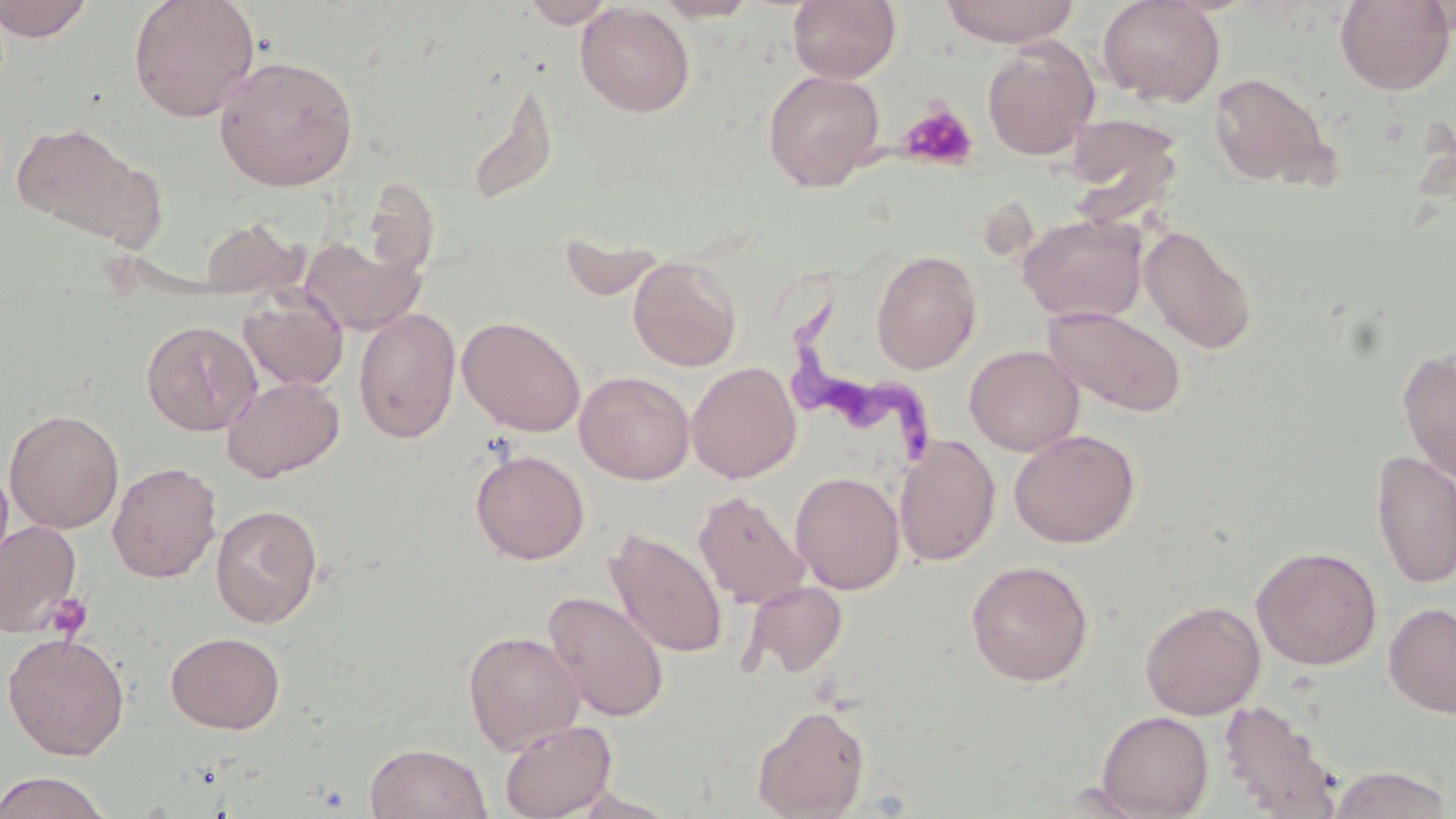
Summary:
  - Coordinate format: approximate bounding boxes as (x1, y1, x2, y2) in pixels
  - Trypanosoma brucei locations: (787, 285, 946, 471)
  - Platelet locations: (898, 101, 979, 171), (47, 592, 93, 641)
  - Uninfected red blood cell locations: (0, 0, 94, 41), (128, 0, 260, 122), (521, 0, 617, 28), (651, 0, 763, 22), (787, 0, 902, 84), (939, 0, 1081, 47), (1097, 0, 1225, 106), (1334, 0, 1455, 94), (575, 3, 695, 117), (981, 36, 1101, 160), (214, 55, 359, 191), (762, 70, 885, 190), (1208, 72, 1335, 189), (465, 82, 559, 207), (1063, 112, 1185, 221), (11, 122, 157, 245), (362, 179, 441, 280), (1017, 214, 1147, 325), (196, 217, 306, 299), (1140, 224, 1257, 355), (559, 235, 667, 302), (302, 238, 425, 335), (870, 250, 982, 374), (628, 257, 742, 372), (238, 291, 348, 392), (1043, 305, 1188, 417), (353, 307, 461, 444), (457, 316, 586, 437), (141, 320, 261, 436), (964, 344, 1084, 456), (1398, 350, 1456, 484), (686, 361, 802, 484), (575, 370, 695, 484), (222, 375, 345, 482), (4, 409, 124, 533), (1009, 429, 1141, 548), (895, 435, 1000, 567), (470, 449, 589, 564), (1371, 450, 1456, 589), (0, 461, 15, 581), (107, 461, 222, 582), (790, 471, 905, 594), (694, 490, 810, 610), (210, 504, 323, 628), (0, 520, 83, 637), (605, 528, 728, 659), (1251, 546, 1382, 670), (966, 559, 1094, 687), (741, 581, 848, 679), (544, 591, 669, 723), (1140, 599, 1265, 719), (1384, 602, 1456, 718), (463, 630, 584, 754), (165, 631, 286, 734), (2, 632, 130, 760), (1219, 699, 1344, 818), (752, 704, 870, 818), (1096, 710, 1214, 818), (500, 719, 617, 819), (365, 743, 492, 819), (1326, 765, 1453, 819), (0, 770, 113, 818)
  - Slide-level diagnosis: Trypanosoma brucei
  - Field of view: one of a larger specimen
  - Preparation: thin blood smear
  - Stain: May-Grünwald-Giemsa
  - Magnification: 1000x
  - Image size: 1456×819 pixels
  - Modality: light microscopy